Identify the parasite.
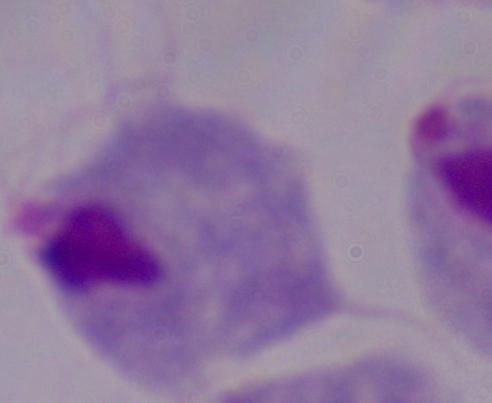

A trichomonad.

1000x magnification. Photomicrograph.